Report the malaria status of this cell.
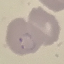
Parasitized.

{
  "image_type": "cell patch, automatically extracted from a larger field of view and resized to 64 × 64 pixels",
  "stain": "Giemsa",
  "capture": "smartphone camera at the microscope eyepiece",
  "preparation": "thin blood smear"
}